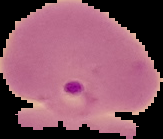

preparation: thin blood smear
result: Plasmodium parasites detected
image_type: segmented cell region with the area outside set to black
image_size: 163×139 pixels